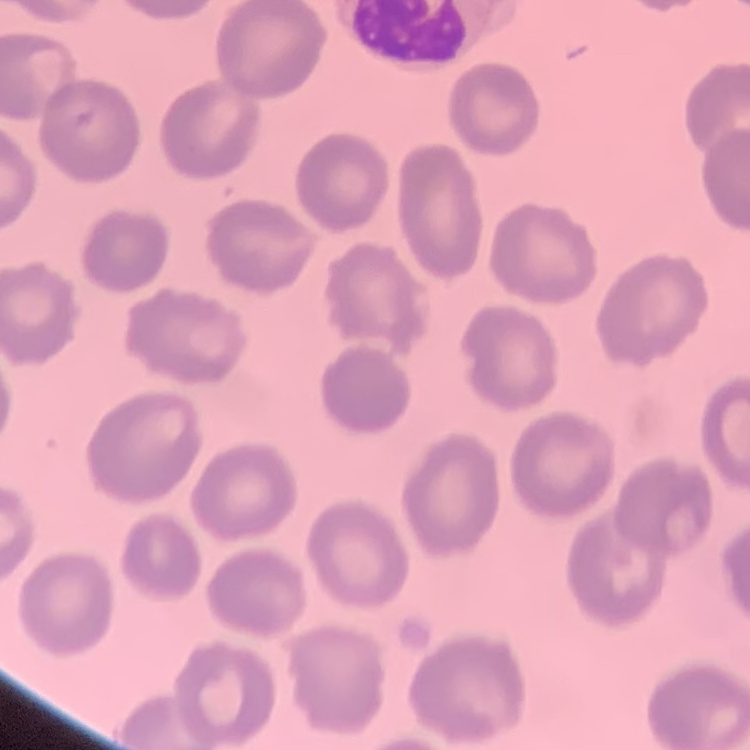 The red blood cells exhibit no rouleaux formation. One tile cut from a larger photomicrograph. Field's or Giemsa stain. Thin blood smear.